Locate every Plasmodium parasite and every leukocyte.
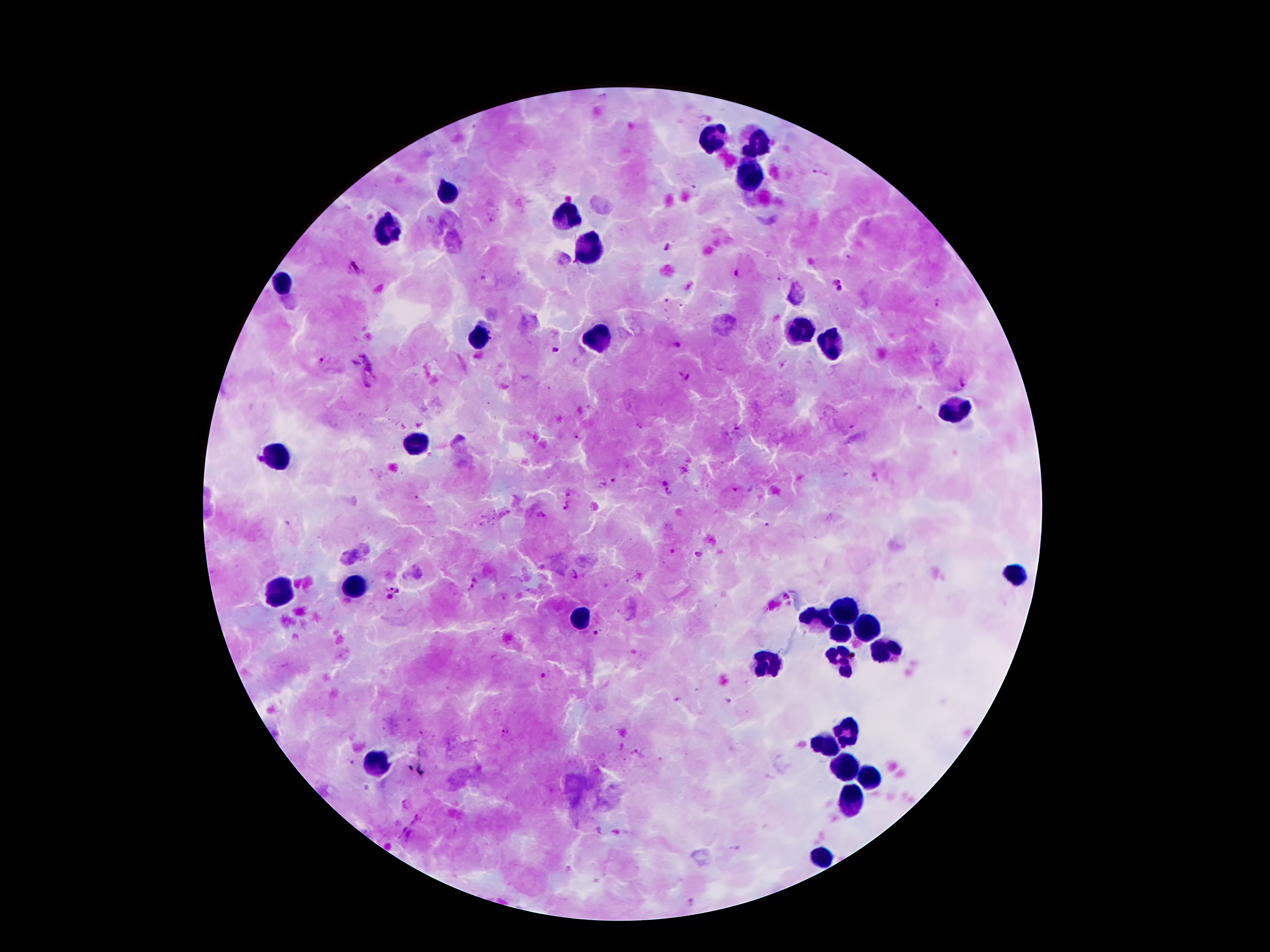

Approximate object centers, in pixels from the top-left corner.
Plasmodium parasites: (x=819, y=173), (x=666, y=247), (x=356, y=267), (x=737, y=273), (x=837, y=283), (x=939, y=303), (x=676, y=347), (x=553, y=350), (x=323, y=360), (x=684, y=377), (x=963, y=381), (x=577, y=436), (x=664, y=482), (x=735, y=490), (x=669, y=491), (x=569, y=494), (x=567, y=506), (x=767, y=525), (x=672, y=552), (x=700, y=554), (x=390, y=586), (x=399, y=592), (x=390, y=596), (x=595, y=633), (x=543, y=676), (x=506, y=733).
Leukocytes: (x=712, y=137), (x=757, y=142), (x=747, y=171), (x=443, y=193), (x=567, y=216), (x=386, y=230), (x=584, y=240), (x=282, y=285), (x=794, y=329), (x=485, y=336), (x=591, y=342), (x=828, y=351), (x=952, y=408), (x=413, y=445), (x=270, y=457), (x=1011, y=573), (x=354, y=586), (x=282, y=591), (x=843, y=610), (x=584, y=618), (x=819, y=618), (x=868, y=625), (x=838, y=633), (x=885, y=650), (x=767, y=659), (x=841, y=663), (x=846, y=732), (x=823, y=744), (x=379, y=760), (x=843, y=768), (x=870, y=778), (x=851, y=796), (x=823, y=855).

Image is 1270×952 pixels. Patient malaria status: positive for Plasmodium falciparum. 100x magnification. Thick blood smear. Photographed through the microscope eyepiece with a smartphone camera. Giemsa-stained preparation. Single field of view.